Locate every leukocyte (white blood cell).
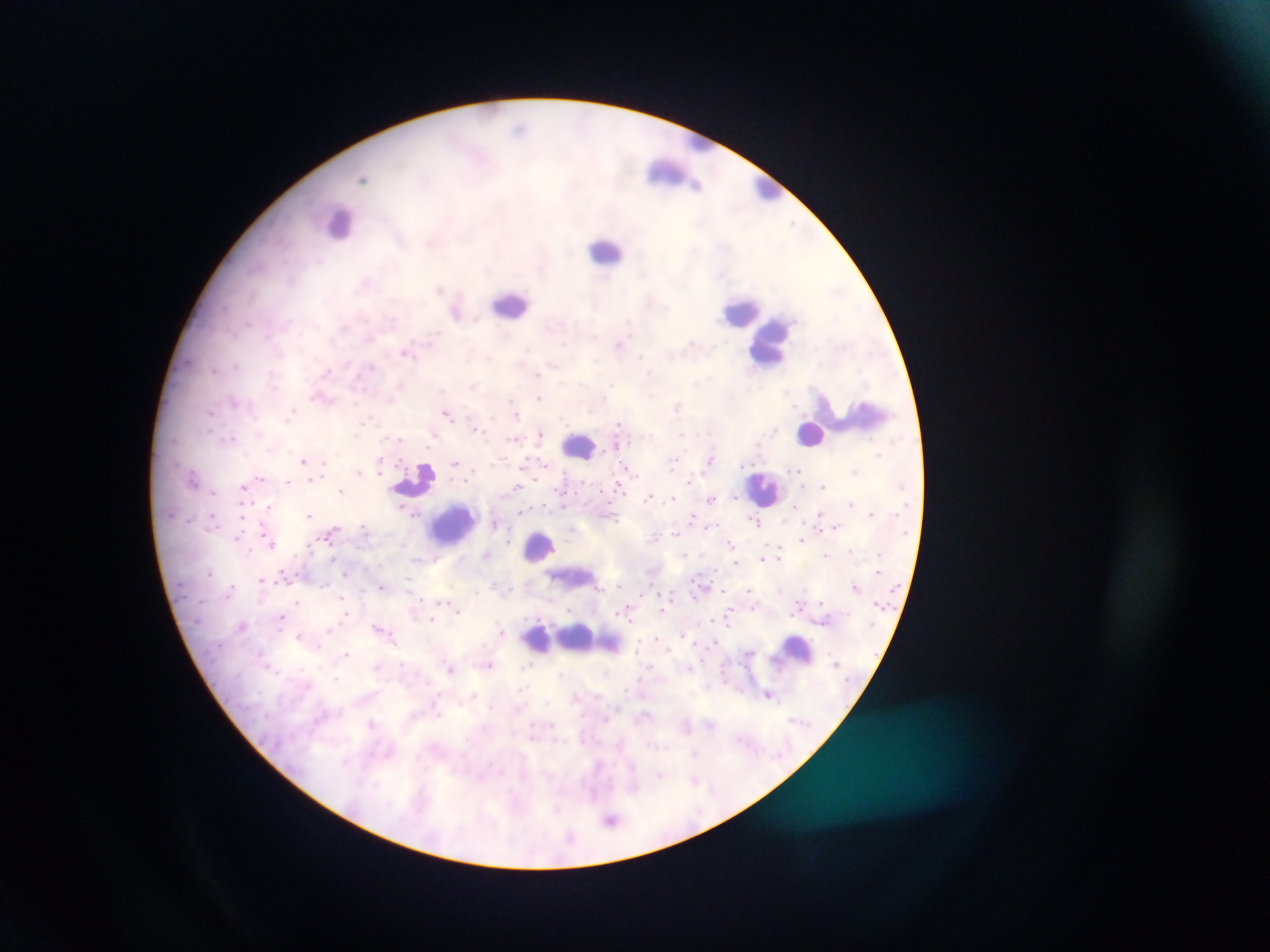

Approximate centers as x y in pixels.
Leukocytes: 700 140; 673 173; 768 188; 340 224; 606 249; 512 302; 742 311; 768 345; 866 415; 811 433; 579 446; 416 478; 765 488; 453 524; 540 548; 573 577; 579 638; 797 650.

country = Ghana
malaria parasite locations = approximate centers as x y in pixels: 519 127; 363 178; 793 224; 440 289; 456 313; 619 345; 407 352; 641 355; 237 365; 552 365; 372 366; 213 371; 327 371; 650 372; 537 375; 274 384; 612 385; 399 386; 788 392; 322 398; 539 398; 389 399; 233 400; 514 404; 677 408; 211 412; 292 412; 447 413; 516 414; 368 421; 618 424; 474 428; 540 433; 231 438; 398 438; 432 438; 513 439; 616 445; 879 454; 710 459; 303 461; 380 461; 455 462; 673 463; 325 464; 545 465; 378 467; 627 468; 797 469; 359 470; 855 471; 193 477; 259 477; 311 479; 689 481; 288 482; 618 486; 823 486; 243 487; 516 487; 341 491; 736 495; 649 496; 674 498; 711 498; 851 503; 562 505; 795 505; 268 506; 241 507; 524 510; 413 514; 871 514; 309 515; 819 515; 213 516; 612 516; 692 516; 755 522; 495 523; 365 525; 836 526; 708 527; 571 531; 331 533; 674 533; 238 536; 656 536; 267 538; 802 539; 508 541; 730 542; 270 543; 850 549; 486 554; 684 554; 826 554; 779 557; 763 558; 333 559; 735 563; 210 573; 345 573; 261 579; 407 579; 324 585; 618 585; 230 587; 382 587; 855 587; 598 588; 749 589; 476 592; 342 597; 297 601; 419 601; 442 602; 821 602; 753 608; 661 609; 570 610; 629 610; 458 611; 731 611; 346 614; 281 617; 432 619; 729 622; 242 626; 329 629; 381 629; 501 631; 299 636; 656 638; 319 648; 346 654; 402 663; 489 665; 527 666; 376 667; 450 667; 689 668; 606 673; 561 674; 336 678; 769 694; 474 695; 372 724; 711 725; 695 752; 660 775; 695 780; 593 792; 557 809; 611 820; 571 837
capture = mobile-phone photograph through a microscope
image size = 1270×952 pixels
preparation = thick blood smear
field of view = single